Outline platelets.
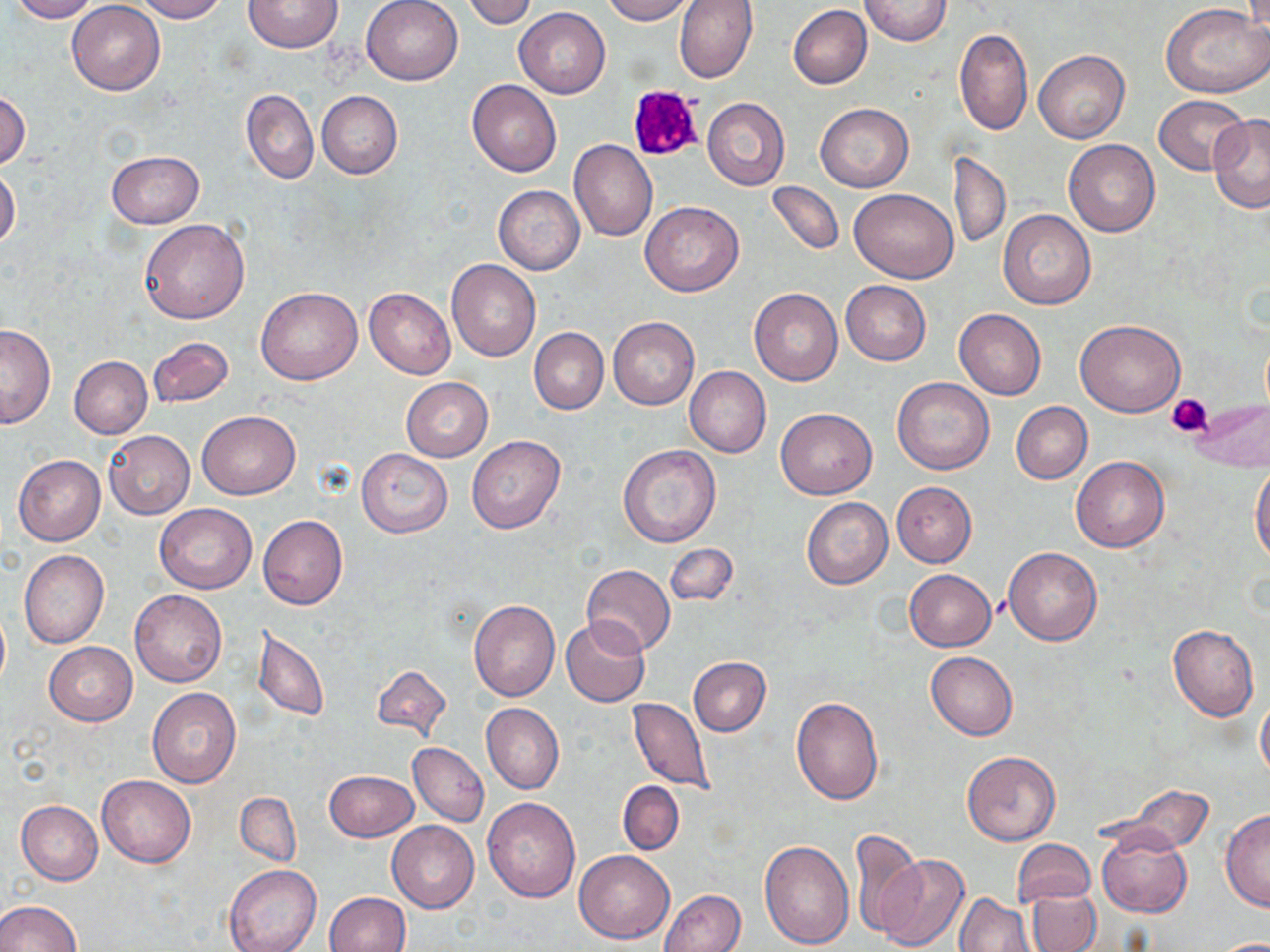

Approximate bounding boxes as named x1/y1/x2/y2 corners in pixels.
Platelets: (x1=628, y1=85, x2=702, y2=162), (x1=1166, y1=394, x2=1213, y2=437).

Summary:
  - Uninfected red blood cell locations: (x1=8, y1=0, x2=100, y2=22), (x1=133, y1=0, x2=230, y2=22), (x1=360, y1=0, x2=463, y2=85), (x1=461, y1=0, x2=536, y2=29), (x1=598, y1=0, x2=694, y2=24), (x1=674, y1=0, x2=758, y2=84), (x1=859, y1=0, x2=954, y2=47), (x1=67, y1=1, x2=165, y2=95), (x1=243, y1=1, x2=344, y2=52), (x1=788, y1=5, x2=872, y2=89), (x1=1163, y1=5, x2=1270, y2=98), (x1=515, y1=7, x2=611, y2=98), (x1=955, y1=28, x2=1032, y2=136), (x1=1034, y1=50, x2=1130, y2=144), (x1=467, y1=80, x2=562, y2=178), (x1=241, y1=89, x2=318, y2=183), (x1=0, y1=90, x2=29, y2=171), (x1=316, y1=90, x2=403, y2=178), (x1=1154, y1=94, x2=1251, y2=176), (x1=702, y1=97, x2=789, y2=191), (x1=816, y1=103, x2=913, y2=192), (x1=1207, y1=114, x2=1270, y2=213), (x1=1063, y1=139, x2=1159, y2=236), (x1=568, y1=140, x2=658, y2=243), (x1=106, y1=150, x2=203, y2=228), (x1=950, y1=151, x2=1010, y2=249), (x1=0, y1=165, x2=20, y2=251), (x1=767, y1=181, x2=843, y2=255), (x1=494, y1=185, x2=584, y2=274), (x1=849, y1=187, x2=959, y2=282), (x1=640, y1=201, x2=744, y2=296), (x1=997, y1=209, x2=1096, y2=309), (x1=139, y1=218, x2=250, y2=324), (x1=446, y1=260, x2=541, y2=361), (x1=841, y1=280, x2=931, y2=365), (x1=257, y1=287, x2=362, y2=384), (x1=364, y1=287, x2=455, y2=379), (x1=749, y1=288, x2=843, y2=386), (x1=953, y1=308, x2=1047, y2=399), (x1=608, y1=317, x2=698, y2=410), (x1=1074, y1=318, x2=1185, y2=417), (x1=0, y1=324, x2=56, y2=428), (x1=529, y1=328, x2=608, y2=414), (x1=146, y1=337, x2=234, y2=408), (x1=69, y1=355, x2=152, y2=438), (x1=685, y1=366, x2=770, y2=457), (x1=400, y1=377, x2=493, y2=462), (x1=892, y1=377, x2=995, y2=475), (x1=1186, y1=398, x2=1270, y2=473), (x1=1011, y1=402, x2=1092, y2=483), (x1=775, y1=408, x2=877, y2=499), (x1=197, y1=410, x2=300, y2=500), (x1=103, y1=431, x2=194, y2=520), (x1=466, y1=434, x2=565, y2=534), (x1=618, y1=444, x2=721, y2=548), (x1=356, y1=448, x2=453, y2=538), (x1=13, y1=454, x2=105, y2=545), (x1=1070, y1=457, x2=1170, y2=552), (x1=1250, y1=466, x2=1270, y2=566), (x1=891, y1=482, x2=977, y2=567), (x1=801, y1=497, x2=892, y2=589), (x1=154, y1=503, x2=257, y2=594), (x1=258, y1=515, x2=348, y2=610), (x1=664, y1=543, x2=737, y2=606), (x1=1003, y1=548, x2=1101, y2=645), (x1=18, y1=549, x2=110, y2=648), (x1=582, y1=564, x2=676, y2=656), (x1=904, y1=569, x2=996, y2=651), (x1=130, y1=589, x2=227, y2=687), (x1=468, y1=600, x2=560, y2=701), (x1=0, y1=607, x2=10, y2=692), (x1=562, y1=618, x2=649, y2=708), (x1=1168, y1=623, x2=1259, y2=721), (x1=251, y1=625, x2=329, y2=723), (x1=44, y1=642, x2=137, y2=725), (x1=926, y1=651, x2=1018, y2=739), (x1=688, y1=656, x2=771, y2=736), (x1=370, y1=664, x2=452, y2=744), (x1=146, y1=686, x2=241, y2=788), (x1=1255, y1=694, x2=1270, y2=780), (x1=629, y1=696, x2=713, y2=792), (x1=790, y1=697, x2=883, y2=805), (x1=481, y1=703, x2=564, y2=793), (x1=409, y1=743, x2=488, y2=825), (x1=962, y1=751, x2=1060, y2=846), (x1=324, y1=770, x2=417, y2=841), (x1=97, y1=774, x2=196, y2=867), (x1=618, y1=781, x2=684, y2=855), (x1=1122, y1=786, x2=1215, y2=853), (x1=235, y1=792, x2=301, y2=866), (x1=483, y1=797, x2=581, y2=902), (x1=16, y1=800, x2=102, y2=885), (x1=1221, y1=810, x2=1270, y2=911), (x1=387, y1=821, x2=479, y2=913), (x1=1098, y1=828, x2=1192, y2=917), (x1=848, y1=830, x2=923, y2=940), (x1=1012, y1=839, x2=1096, y2=905), (x1=759, y1=840, x2=854, y2=948), (x1=574, y1=849, x2=675, y2=944), (x1=873, y1=853, x2=971, y2=951), (x1=224, y1=864, x2=321, y2=952), (x1=660, y1=889, x2=745, y2=952), (x1=1027, y1=889, x2=1101, y2=952), (x1=324, y1=891, x2=409, y2=952), (x1=955, y1=892, x2=1036, y2=952), (x1=0, y1=900, x2=80, y2=952), (x1=1212, y1=939, x2=1269, y2=952)
  - Slide-level diagnosis: no evidence of blood parasites
  - Field of view: single
  - Magnification: 1000x
  - Preparation: thin blood film
  - Stain: May-Grünwald-Giemsa
  - Image size: 1270×952 pixels
  - Modality: optical microscopy